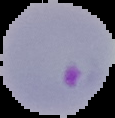

Summary:
  - Preparation: thin blood film
  - Result: malaria parasites detected
  - Image type: cell region segmented out of the field of view; surrounding area masked to black
  - Image size: 115×118 pixels